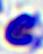

400x magnification. A leukocyte is shown. Micrograph.